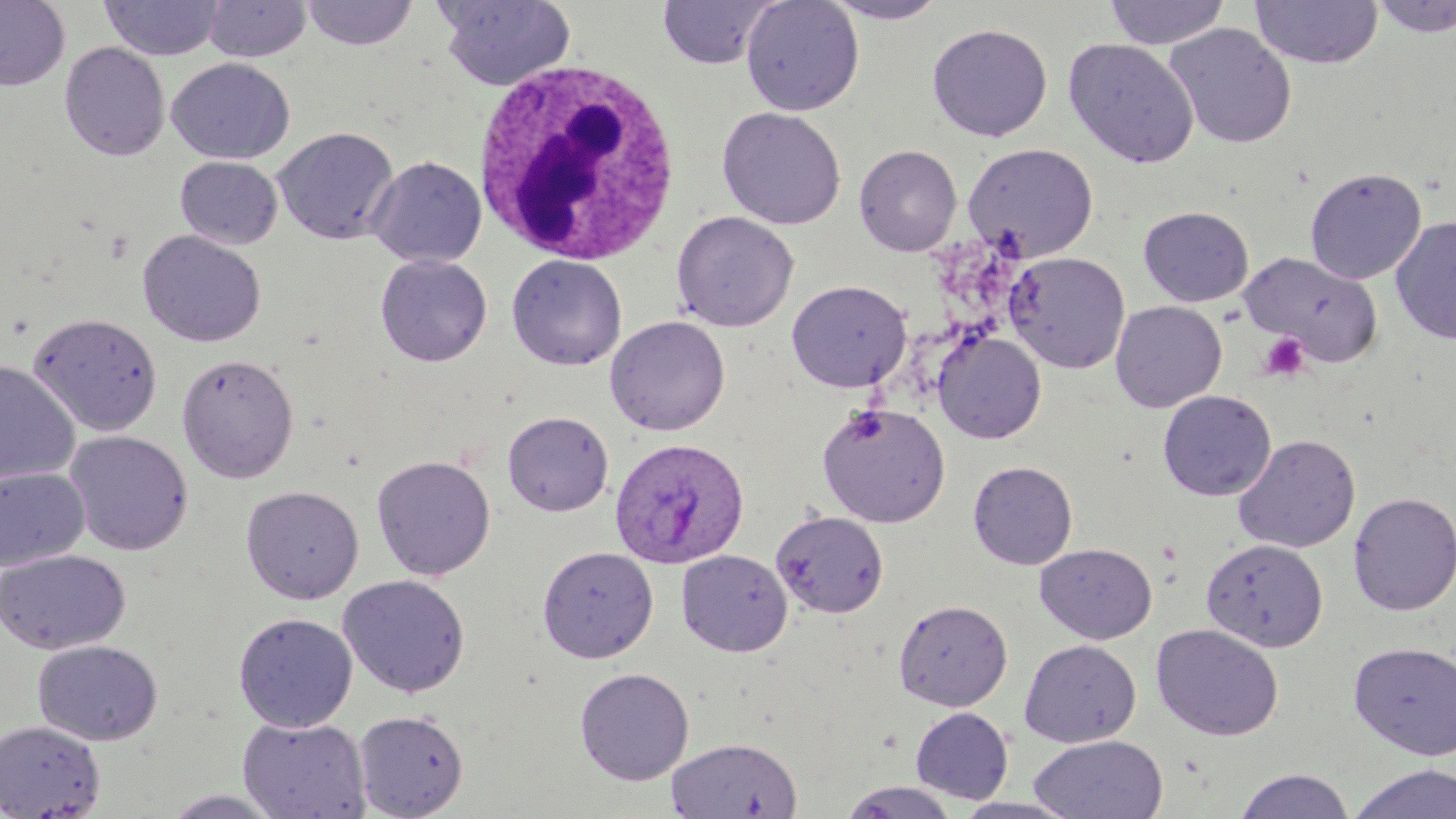

Summary:
  - Coordinate format: approximate bounding boxes as (x1, y1, x2, y2) in pixels
  - White blood cell locations: (471, 58, 685, 263)
  - Uninfected red blood cell locations: (0, 0, 70, 91), (437, 0, 576, 91), (657, 0, 777, 69), (740, 0, 864, 116), (820, 0, 951, 24), (1104, 0, 1231, 49), (1250, 0, 1383, 69), (1369, 0, 1456, 38), (99, 1, 225, 61), (203, 1, 312, 62), (301, 1, 419, 50), (1163, 22, 1298, 149), (927, 23, 1053, 141), (1063, 37, 1199, 168), (59, 42, 169, 161), (167, 58, 295, 165), (716, 106, 846, 230), (272, 126, 399, 245), (963, 142, 1099, 261), (854, 144, 962, 256), (367, 155, 487, 268), (175, 156, 283, 249), (1304, 166, 1427, 284), (1138, 206, 1254, 307), (1130, 207, 1242, 415), (671, 210, 799, 332), (1391, 216, 1456, 344), (137, 230, 266, 347), (1239, 251, 1385, 367), (1004, 252, 1130, 373), (506, 253, 628, 371), (374, 254, 493, 367), (786, 279, 912, 393), (1110, 300, 1227, 412), (27, 312, 163, 436), (605, 315, 731, 436), (933, 330, 1046, 444), (177, 353, 299, 483), (0, 359, 80, 486), (1157, 389, 1277, 501), (816, 402, 950, 527), (502, 410, 614, 516), (63, 430, 193, 556), (1233, 434, 1361, 553), (370, 454, 495, 581), (968, 460, 1078, 569), (0, 467, 90, 572), (240, 485, 364, 604), (1348, 492, 1456, 616), (771, 510, 889, 619), (1201, 538, 1328, 652), (1035, 543, 1157, 644), (536, 545, 659, 662), (0, 548, 131, 655), (676, 549, 793, 657), (336, 574, 471, 698), (893, 599, 1013, 711), (234, 612, 358, 732), (1150, 623, 1284, 741), (1019, 639, 1141, 747), (32, 640, 163, 745), (1348, 640, 1456, 760), (574, 666, 695, 785), (910, 707, 1014, 804), (353, 709, 469, 818), (237, 716, 370, 819), (0, 720, 106, 818), (1028, 734, 1169, 819), (666, 737, 803, 818), (1346, 763, 1456, 819), (1233, 768, 1356, 819), (837, 782, 964, 818), (160, 789, 288, 818), (951, 796, 1080, 818)
  - Plasmodium ovale-infected red blood cell locations: (609, 436, 749, 569)
  - Platelet locations: (1258, 332, 1311, 382)
  - Slide-level diagnosis: Plasmodium ovale
  - Stain: May-Grünwald-Giemsa
  - Magnification: 1000x
  - Modality: light microscopy
  - Preparation: thin blood smear
  - Field of view: one of a larger specimen
  - Image size: 1456×819 pixels